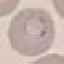 Malaria status: uninfected. Photographed with a smartphone camera at the microscope eyepiece. Giemsa-stained preparation. Thin blood smear. Automatically extracted cell patch, resized to 64 × 64 pixels.